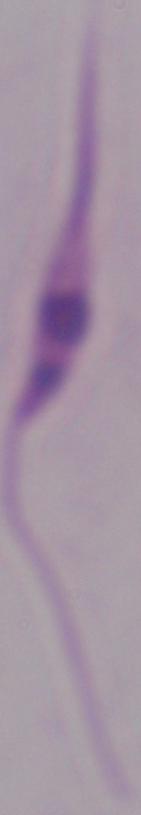

identification = Leishmania
modality = micrograph
magnification = 1000x